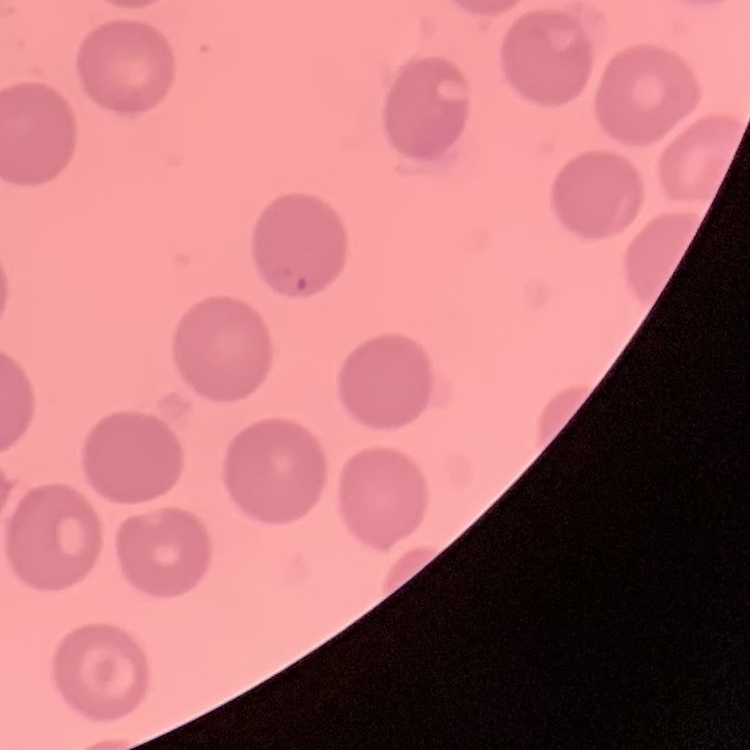

The erythrocytes exhibit no rouleaux formation. Stained with either Field's or Giemsa. Square crop of a larger photomicrograph. Thin peripheral smear.